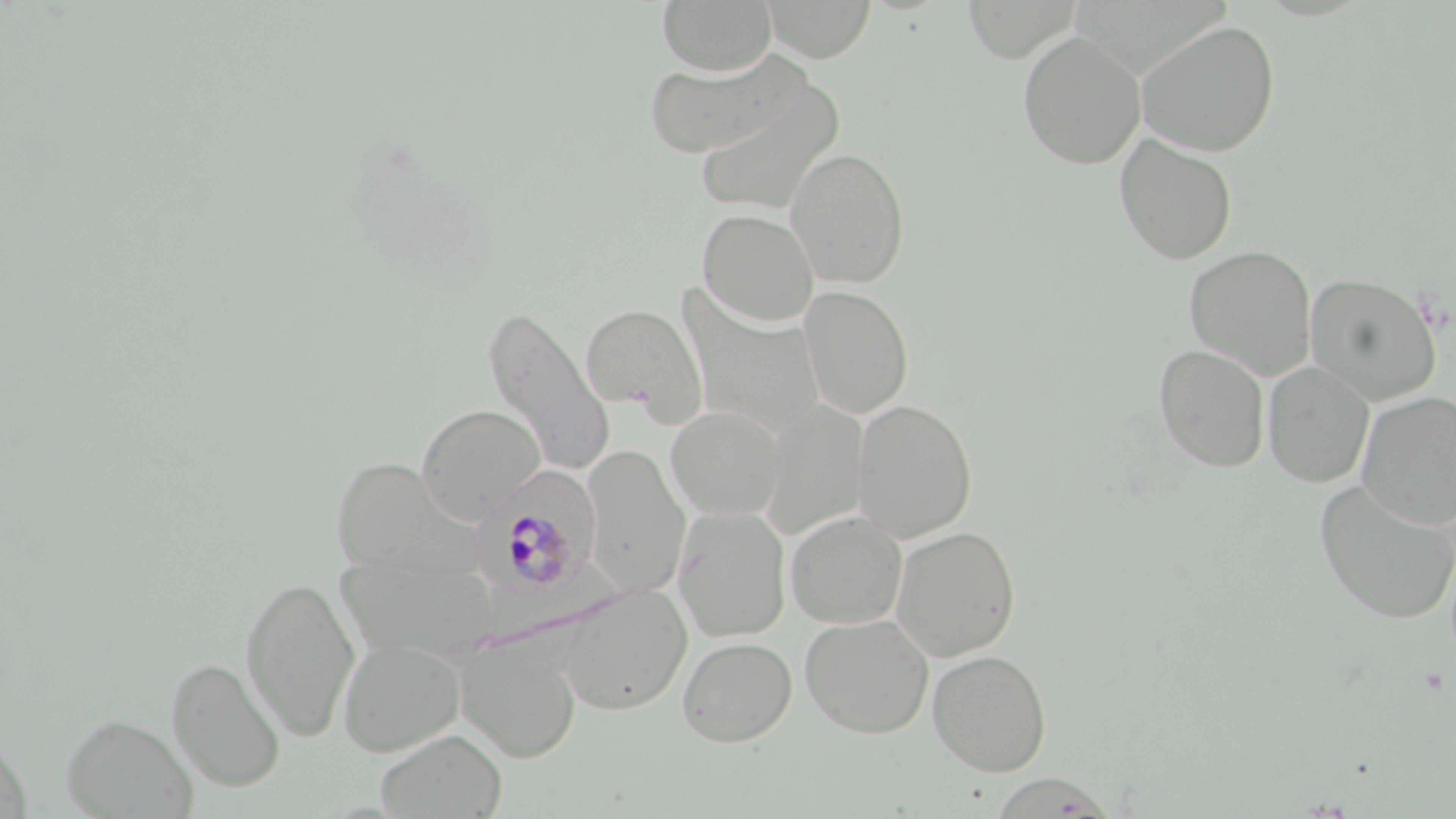
Approximate bounding boxes as named x1/y1/x2/y2 corners in pixels. Uninfected red blood cell locations: (x1=657, y1=0, x2=776, y2=75), (x1=762, y1=0, x2=876, y2=62), (x1=962, y1=0, x2=1081, y2=63), (x1=1136, y1=19, x2=1280, y2=156), (x1=1017, y1=30, x2=1146, y2=169), (x1=643, y1=51, x2=805, y2=159), (x1=691, y1=83, x2=845, y2=216), (x1=1114, y1=133, x2=1237, y2=264), (x1=786, y1=146, x2=911, y2=287), (x1=697, y1=208, x2=819, y2=328), (x1=1185, y1=245, x2=1317, y2=380), (x1=1305, y1=272, x2=1442, y2=404), (x1=799, y1=285, x2=913, y2=419), (x1=680, y1=297, x2=826, y2=441), (x1=581, y1=304, x2=707, y2=423), (x1=482, y1=306, x2=615, y2=477), (x1=1153, y1=343, x2=1270, y2=473), (x1=1263, y1=361, x2=1374, y2=487), (x1=1357, y1=391, x2=1456, y2=530), (x1=758, y1=398, x2=867, y2=539), (x1=852, y1=398, x2=977, y2=543), (x1=416, y1=404, x2=545, y2=523), (x1=666, y1=405, x2=786, y2=521), (x1=583, y1=445, x2=690, y2=597), (x1=330, y1=457, x2=473, y2=580), (x1=1314, y1=479, x2=1456, y2=624), (x1=674, y1=506, x2=792, y2=642), (x1=785, y1=510, x2=908, y2=629), (x1=891, y1=525, x2=1021, y2=662), (x1=334, y1=560, x2=499, y2=667), (x1=240, y1=573, x2=360, y2=742), (x1=558, y1=584, x2=692, y2=715), (x1=799, y1=613, x2=934, y2=738), (x1=678, y1=636, x2=797, y2=747), (x1=338, y1=637, x2=465, y2=757), (x1=457, y1=639, x2=581, y2=762), (x1=927, y1=649, x2=1052, y2=775), (x1=166, y1=656, x2=285, y2=792), (x1=60, y1=712, x2=198, y2=819), (x1=0, y1=729, x2=32, y2=818), (x1=376, y1=729, x2=507, y2=818). Plasmodium malariae-infected red blood cell locations: (x1=471, y1=474, x2=597, y2=601). Slide-level diagnosis: Plasmodium malariae. Thin blood film. May-Grünwald-Giemsa stain. Single field of view. Light microscopy. Image is 1456×819 pixels. 1000x magnification.